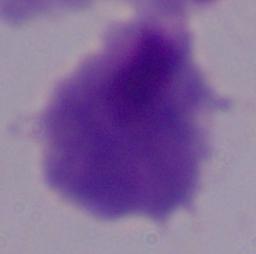

Micrograph. A trichomonad is shown. 1000x magnification.